State the blood parasite species.
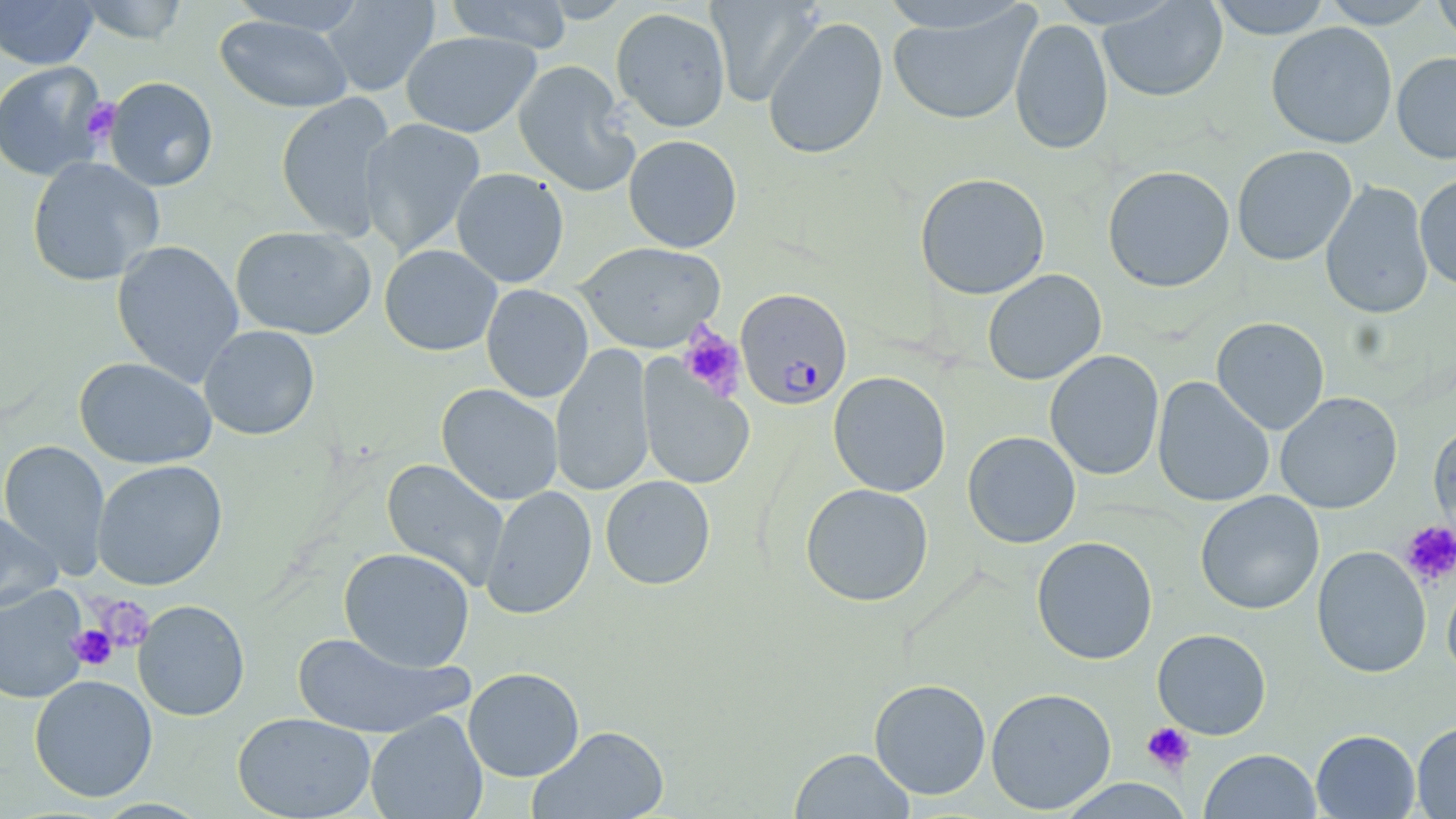
Plasmodium falciparum.

Summary:
  - Coordinate format: approximate bounding boxes as named x1/y1/x2/y2 corners in pixels
  - Uninfected red blood cell locations: (x1=0, y1=0, x2=99, y2=69), (x1=76, y1=0, x2=190, y2=43), (x1=321, y1=0, x2=439, y2=96), (x1=442, y1=0, x2=575, y2=53), (x1=706, y1=0, x2=821, y2=107), (x1=1207, y1=0, x2=1333, y2=39), (x1=1320, y1=0, x2=1438, y2=28), (x1=1432, y1=0, x2=1456, y2=50), (x1=226, y1=1, x2=372, y2=35), (x1=1098, y1=1, x2=1228, y2=103), (x1=887, y1=6, x2=1040, y2=126), (x1=611, y1=7, x2=731, y2=132), (x1=215, y1=14, x2=354, y2=113), (x1=763, y1=16, x2=888, y2=160), (x1=1009, y1=18, x2=1113, y2=155), (x1=1266, y1=22, x2=1398, y2=149), (x1=401, y1=31, x2=542, y2=138), (x1=1391, y1=52, x2=1456, y2=164), (x1=513, y1=60, x2=639, y2=197), (x1=0, y1=61, x2=110, y2=181), (x1=101, y1=76, x2=219, y2=192), (x1=275, y1=92, x2=397, y2=241), (x1=359, y1=117, x2=486, y2=259), (x1=623, y1=134, x2=742, y2=252), (x1=1232, y1=145, x2=1357, y2=266), (x1=26, y1=156, x2=165, y2=287), (x1=1102, y1=165, x2=1235, y2=293), (x1=451, y1=167, x2=570, y2=288), (x1=914, y1=172, x2=1050, y2=300), (x1=1415, y1=173, x2=1456, y2=290), (x1=1320, y1=181, x2=1434, y2=320), (x1=230, y1=225, x2=377, y2=340), (x1=111, y1=240, x2=245, y2=386), (x1=574, y1=241, x2=726, y2=353), (x1=379, y1=244, x2=503, y2=356), (x1=982, y1=269, x2=1107, y2=386), (x1=481, y1=284, x2=594, y2=403), (x1=1211, y1=317, x2=1330, y2=435), (x1=198, y1=324, x2=320, y2=440), (x1=550, y1=343, x2=655, y2=498), (x1=1044, y1=350, x2=1164, y2=480), (x1=74, y1=356, x2=217, y2=469), (x1=637, y1=357, x2=756, y2=491), (x1=828, y1=371, x2=951, y2=497), (x1=1152, y1=377, x2=1274, y2=508), (x1=436, y1=383, x2=564, y2=505), (x1=1275, y1=392, x2=1403, y2=514), (x1=1429, y1=420, x2=1456, y2=548), (x1=963, y1=431, x2=1081, y2=548), (x1=0, y1=440, x2=111, y2=577), (x1=381, y1=458, x2=510, y2=592), (x1=92, y1=459, x2=229, y2=590), (x1=600, y1=475, x2=716, y2=590), (x1=800, y1=483, x2=934, y2=607), (x1=480, y1=485, x2=597, y2=620), (x1=1195, y1=490, x2=1324, y2=615), (x1=0, y1=510, x2=63, y2=613), (x1=1031, y1=536, x2=1158, y2=665), (x1=1312, y1=545, x2=1432, y2=679), (x1=338, y1=547, x2=476, y2=671), (x1=1442, y1=560, x2=1456, y2=684), (x1=0, y1=585, x2=89, y2=705), (x1=133, y1=600, x2=250, y2=721), (x1=1152, y1=629, x2=1271, y2=739), (x1=292, y1=631, x2=471, y2=740), (x1=463, y1=667, x2=584, y2=781), (x1=29, y1=674, x2=158, y2=802), (x1=869, y1=678, x2=991, y2=799), (x1=986, y1=687, x2=1116, y2=814), (x1=365, y1=710, x2=488, y2=819), (x1=232, y1=712, x2=377, y2=818), (x1=1412, y1=720, x2=1456, y2=818), (x1=529, y1=725, x2=669, y2=819), (x1=1311, y1=729, x2=1420, y2=817), (x1=790, y1=747, x2=914, y2=819), (x1=1200, y1=749, x2=1322, y2=819), (x1=1056, y1=778, x2=1195, y2=818)
  - Plasmodium falciparum-infected red blood cell locations: (x1=735, y1=288, x2=852, y2=410)
  - Platelet locations: (x1=81, y1=97, x2=121, y2=144), (x1=678, y1=325, x2=746, y2=401), (x1=1399, y1=520, x2=1456, y2=588), (x1=91, y1=595, x2=154, y2=653), (x1=68, y1=624, x2=118, y2=671), (x1=1142, y1=722, x2=1195, y2=773)
  - Magnification: 1000x
  - Image size: 1456×819 pixels
  - Stain: May-Grünwald-Giemsa
  - Preparation: thin blood smear
  - Field of view: single
  - Modality: light microscopy